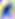
{
  "modality": "photomicrograph",
  "identification": "Toxoplasma gondii",
  "magnification": "400x"
}